Assess this cell for malaria.
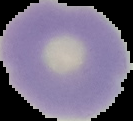
It is uninfected.

Summary:
  - Image size: 133×121 pixels
  - Image type: segmented cell region on a black background
  - Preparation: thin blood smear